Locate and identify every blood parasite.
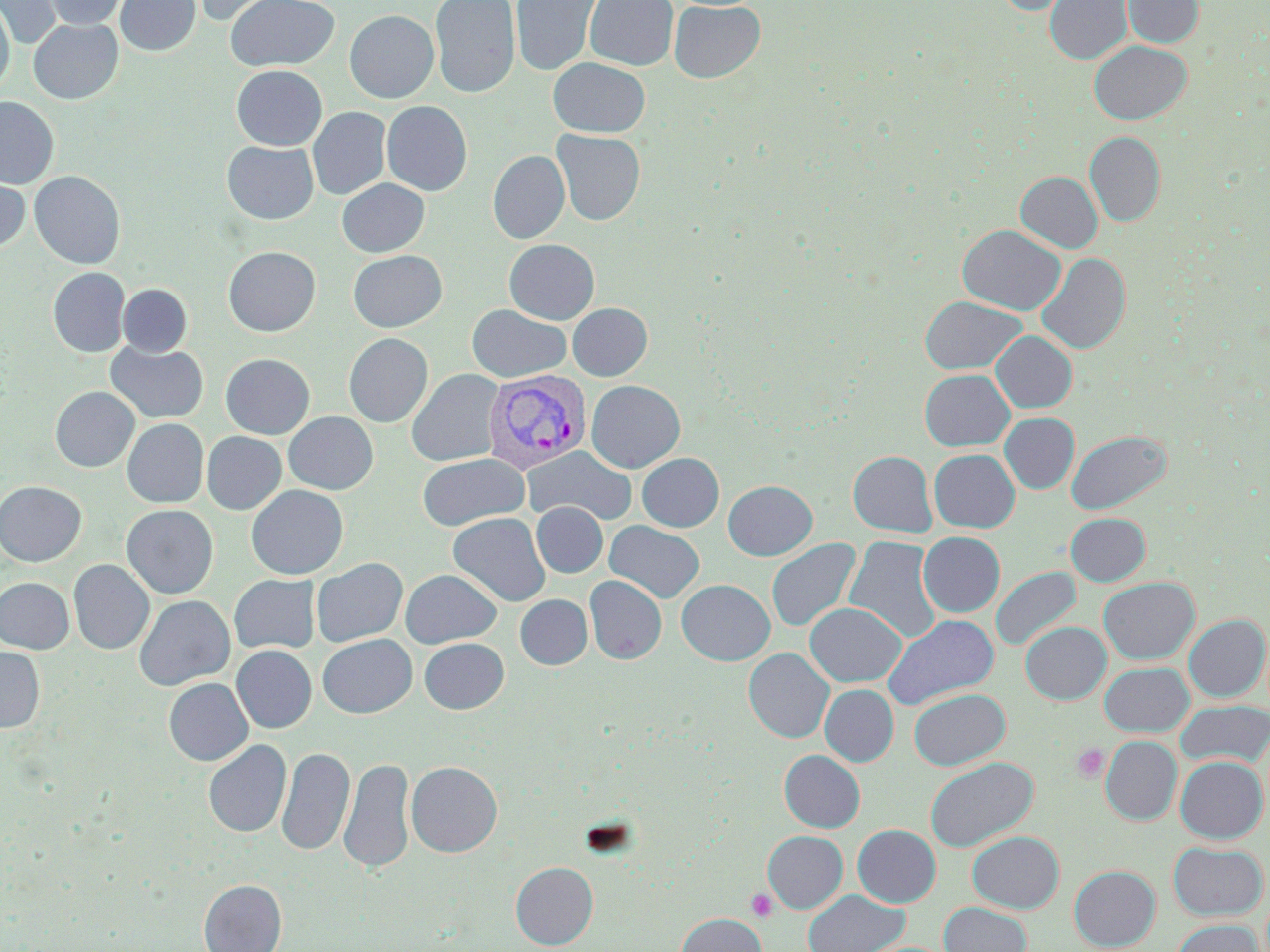

Approximate bounding boxes as named x1/y1/x2/y2 corners in pixels.
Plasmodium vivax-infected red blood cells: (x1=483, y1=370, x2=590, y2=474).
No Plasmodium falciparum, Plasmodium ovale, Plasmodium malariae, Babesia divergens, or Trypanosoma brucei observed.

Summary:
  - Platelet locations: (x1=1071, y1=744, x2=1109, y2=783), (x1=745, y1=888, x2=778, y2=922)
  - Uninfected red blood cell locations: (x1=0, y1=0, x2=62, y2=49), (x1=42, y1=0, x2=127, y2=30), (x1=114, y1=0, x2=200, y2=57), (x1=185, y1=0, x2=290, y2=26), (x1=225, y1=0, x2=339, y2=71), (x1=430, y1=0, x2=520, y2=99), (x1=510, y1=0, x2=603, y2=77), (x1=584, y1=0, x2=679, y2=70), (x1=996, y1=0, x2=1073, y2=15), (x1=1045, y1=0, x2=1132, y2=65), (x1=1123, y1=0, x2=1203, y2=48), (x1=669, y1=1, x2=765, y2=83), (x1=0, y1=3, x2=14, y2=96), (x1=345, y1=10, x2=439, y2=103), (x1=28, y1=18, x2=123, y2=104), (x1=1089, y1=40, x2=1191, y2=124), (x1=548, y1=57, x2=650, y2=138), (x1=231, y1=65, x2=327, y2=150), (x1=0, y1=96, x2=59, y2=188), (x1=382, y1=101, x2=472, y2=196), (x1=307, y1=107, x2=391, y2=200), (x1=551, y1=129, x2=645, y2=226), (x1=1085, y1=132, x2=1165, y2=227), (x1=222, y1=141, x2=318, y2=224), (x1=488, y1=150, x2=570, y2=244), (x1=29, y1=171, x2=125, y2=269), (x1=1015, y1=171, x2=1103, y2=253), (x1=0, y1=173, x2=30, y2=253), (x1=337, y1=178, x2=429, y2=257), (x1=957, y1=224, x2=1066, y2=315), (x1=504, y1=239, x2=599, y2=324), (x1=223, y1=246, x2=321, y2=336), (x1=348, y1=250, x2=447, y2=332), (x1=1036, y1=252, x2=1130, y2=355), (x1=48, y1=267, x2=130, y2=357), (x1=118, y1=284, x2=192, y2=356), (x1=919, y1=296, x2=1027, y2=374), (x1=568, y1=302, x2=652, y2=381), (x1=467, y1=304, x2=571, y2=383), (x1=992, y1=330, x2=1077, y2=413), (x1=344, y1=333, x2=433, y2=427), (x1=106, y1=341, x2=208, y2=423), (x1=220, y1=353, x2=315, y2=439), (x1=407, y1=368, x2=504, y2=467), (x1=919, y1=369, x2=1014, y2=451), (x1=586, y1=380, x2=685, y2=473), (x1=50, y1=386, x2=139, y2=472), (x1=283, y1=411, x2=378, y2=494), (x1=999, y1=412, x2=1079, y2=494), (x1=122, y1=418, x2=209, y2=508), (x1=1065, y1=429, x2=1171, y2=515), (x1=202, y1=432, x2=287, y2=514), (x1=522, y1=446, x2=636, y2=526), (x1=929, y1=449, x2=1020, y2=532), (x1=848, y1=451, x2=937, y2=537), (x1=417, y1=453, x2=529, y2=531), (x1=637, y1=453, x2=724, y2=531), (x1=723, y1=480, x2=817, y2=560), (x1=0, y1=481, x2=86, y2=566), (x1=246, y1=485, x2=348, y2=579), (x1=532, y1=502, x2=607, y2=577), (x1=121, y1=505, x2=218, y2=598), (x1=448, y1=512, x2=550, y2=607), (x1=1065, y1=512, x2=1150, y2=586), (x1=604, y1=520, x2=705, y2=603), (x1=918, y1=532, x2=1005, y2=617), (x1=844, y1=535, x2=942, y2=643), (x1=766, y1=538, x2=861, y2=634), (x1=311, y1=558, x2=408, y2=647), (x1=68, y1=560, x2=154, y2=654), (x1=990, y1=567, x2=1081, y2=652), (x1=400, y1=568, x2=502, y2=648), (x1=229, y1=574, x2=320, y2=654), (x1=585, y1=575, x2=667, y2=665), (x1=0, y1=577, x2=74, y2=653), (x1=1098, y1=577, x2=1199, y2=664), (x1=676, y1=579, x2=775, y2=665), (x1=133, y1=595, x2=235, y2=690), (x1=515, y1=595, x2=592, y2=669), (x1=804, y1=602, x2=906, y2=686), (x1=882, y1=614, x2=999, y2=710), (x1=1184, y1=614, x2=1269, y2=701), (x1=1021, y1=621, x2=1111, y2=704), (x1=317, y1=633, x2=417, y2=718), (x1=419, y1=638, x2=509, y2=713), (x1=232, y1=645, x2=316, y2=733), (x1=0, y1=647, x2=45, y2=732), (x1=743, y1=647, x2=834, y2=743), (x1=1099, y1=662, x2=1193, y2=736), (x1=163, y1=678, x2=253, y2=765), (x1=820, y1=684, x2=898, y2=766), (x1=909, y1=688, x2=1010, y2=770), (x1=1175, y1=701, x2=1270, y2=768), (x1=1100, y1=736, x2=1182, y2=824), (x1=203, y1=739, x2=291, y2=838), (x1=276, y1=746, x2=354, y2=857), (x1=779, y1=750, x2=865, y2=832), (x1=338, y1=755, x2=415, y2=875), (x1=1175, y1=756, x2=1267, y2=843), (x1=924, y1=757, x2=1038, y2=852), (x1=406, y1=761, x2=502, y2=857), (x1=853, y1=824, x2=941, y2=907), (x1=763, y1=830, x2=848, y2=913), (x1=967, y1=831, x2=1064, y2=913), (x1=1168, y1=842, x2=1267, y2=920), (x1=511, y1=861, x2=598, y2=949), (x1=1069, y1=865, x2=1160, y2=950), (x1=199, y1=879, x2=286, y2=952), (x1=803, y1=889, x2=908, y2=952), (x1=939, y1=902, x2=1031, y2=952), (x1=676, y1=912, x2=766, y2=952), (x1=1172, y1=919, x2=1264, y2=952)
  - Slide-level diagnosis: Plasmodium vivax
  - Magnification: 1000x
  - Preparation: thin blood film
  - Modality: light microscopy
  - Stain: May-Grünwald-Giemsa
  - Image size: 1270×952 pixels
  - Field of view: one of a larger specimen